Locate every blood parasite and identify its species.
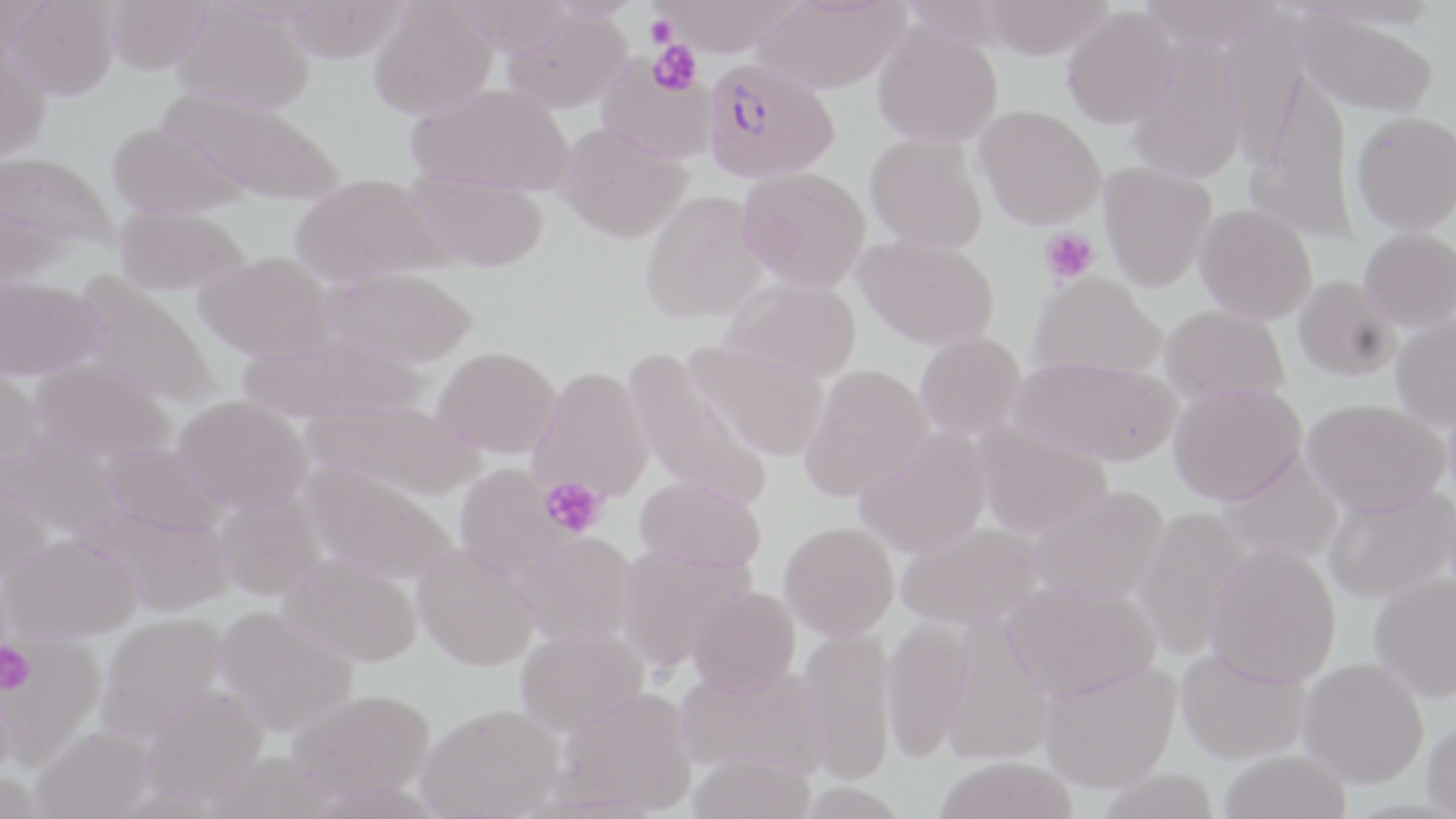

Approximate bounding boxes as [x1, y1, x2, y2] in pixels.
Plasmodium falciparum-infected red blood cells: [702, 57, 839, 184].
No Plasmodium ovale, Plasmodium malariae, Plasmodium vivax, Babesia divergens, or Trypanosoma brucei observed.

Summary:
  - Uninfected red blood cell locations: [8, 0, 119, 100], [105, 0, 214, 76], [368, 0, 497, 121], [656, 0, 804, 57], [752, 0, 907, 95], [982, 0, 1114, 59], [1138, 0, 1286, 49], [172, 1, 315, 116], [1061, 7, 1179, 129], [503, 8, 632, 113], [1294, 8, 1440, 118], [873, 20, 1004, 147], [1127, 41, 1247, 184], [0, 46, 51, 163], [596, 55, 716, 164], [407, 83, 576, 196], [160, 89, 344, 206], [974, 104, 1106, 230], [1351, 111, 1456, 235], [106, 120, 244, 219], [557, 123, 691, 245], [865, 133, 988, 253], [1, 152, 119, 255], [1098, 162, 1217, 291], [737, 166, 871, 292], [405, 172, 550, 273], [290, 173, 448, 286], [639, 190, 770, 325], [0, 201, 69, 294], [1194, 204, 1317, 324], [114, 206, 249, 298], [1359, 227, 1456, 331], [854, 235, 1000, 350], [194, 251, 336, 363], [322, 265, 478, 368], [1028, 273, 1166, 382], [74, 275, 220, 409], [1293, 275, 1399, 382], [0, 278, 107, 383], [718, 278, 862, 383], [1159, 305, 1290, 406], [1390, 314, 1456, 430], [914, 331, 1026, 441], [239, 332, 424, 425], [681, 336, 830, 461], [432, 346, 563, 458], [622, 347, 772, 514], [1012, 355, 1181, 468], [0, 360, 44, 473], [30, 360, 175, 463], [798, 364, 933, 502], [528, 365, 655, 501], [1168, 382, 1305, 505], [173, 395, 313, 515], [304, 398, 483, 502], [1301, 398, 1449, 516], [970, 418, 1113, 540], [0, 426, 125, 538], [853, 428, 992, 558], [99, 442, 231, 537], [1216, 451, 1344, 566], [301, 463, 456, 585], [453, 464, 576, 579], [0, 476, 53, 586], [634, 476, 766, 573], [1323, 484, 1456, 605], [1027, 485, 1169, 605], [215, 490, 328, 601], [77, 504, 235, 618], [1131, 507, 1254, 659], [779, 521, 899, 641], [896, 522, 1043, 630], [515, 531, 639, 644], [2, 534, 142, 642], [412, 543, 539, 671], [1205, 543, 1342, 687], [615, 544, 754, 671], [278, 552, 423, 667], [1368, 571, 1456, 702], [1001, 579, 1160, 701], [686, 586, 801, 698], [213, 605, 358, 736], [96, 613, 228, 743], [881, 616, 970, 762], [515, 626, 649, 736], [798, 627, 897, 784], [1174, 646, 1310, 765], [1298, 657, 1429, 788], [1038, 659, 1180, 793], [675, 662, 825, 779], [142, 683, 269, 804], [552, 686, 698, 815], [285, 688, 434, 802], [417, 703, 565, 819], [1421, 716, 1456, 818], [31, 724, 156, 819], [1217, 749, 1352, 819], [203, 750, 334, 819], [687, 751, 817, 819], [932, 757, 1079, 819], [1093, 768, 1222, 819]
  - Platelet locations: [645, 15, 677, 48], [648, 39, 703, 95], [1040, 227, 1099, 285], [539, 477, 608, 538], [0, 641, 36, 695]
  - Slide-level diagnosis: Plasmodium falciparum
  - Stain: May-Grünwald-Giemsa
  - Preparation: thin blood smear
  - Image size: 1456×819 pixels
  - Magnification: 1000x
  - Field of view: one of a larger specimen
  - Modality: optical microscopy